Comment on the morphology of the erythrocytes.
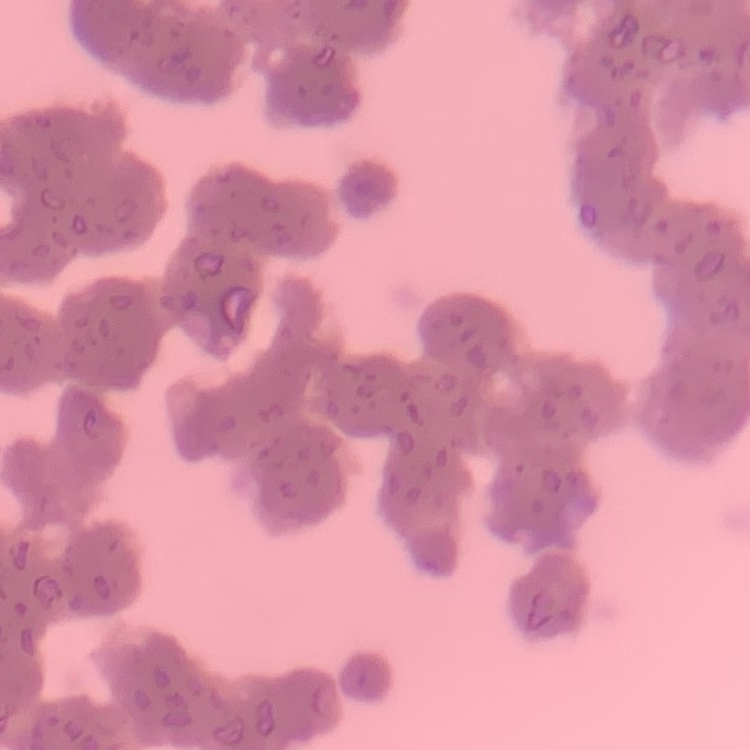
Rouleaux formation.

Summary:
  - Stain: Field's or Giemsa
  - Preparation: thin blood film
  - Image type: one tile cut from a larger photomicrograph